Report the malaria status of this cell.
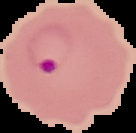

Parasitized.

Image is 136×133 pixels. From a thin blood film. The area outside the segmented cell region is set to black.